State the preparation type.
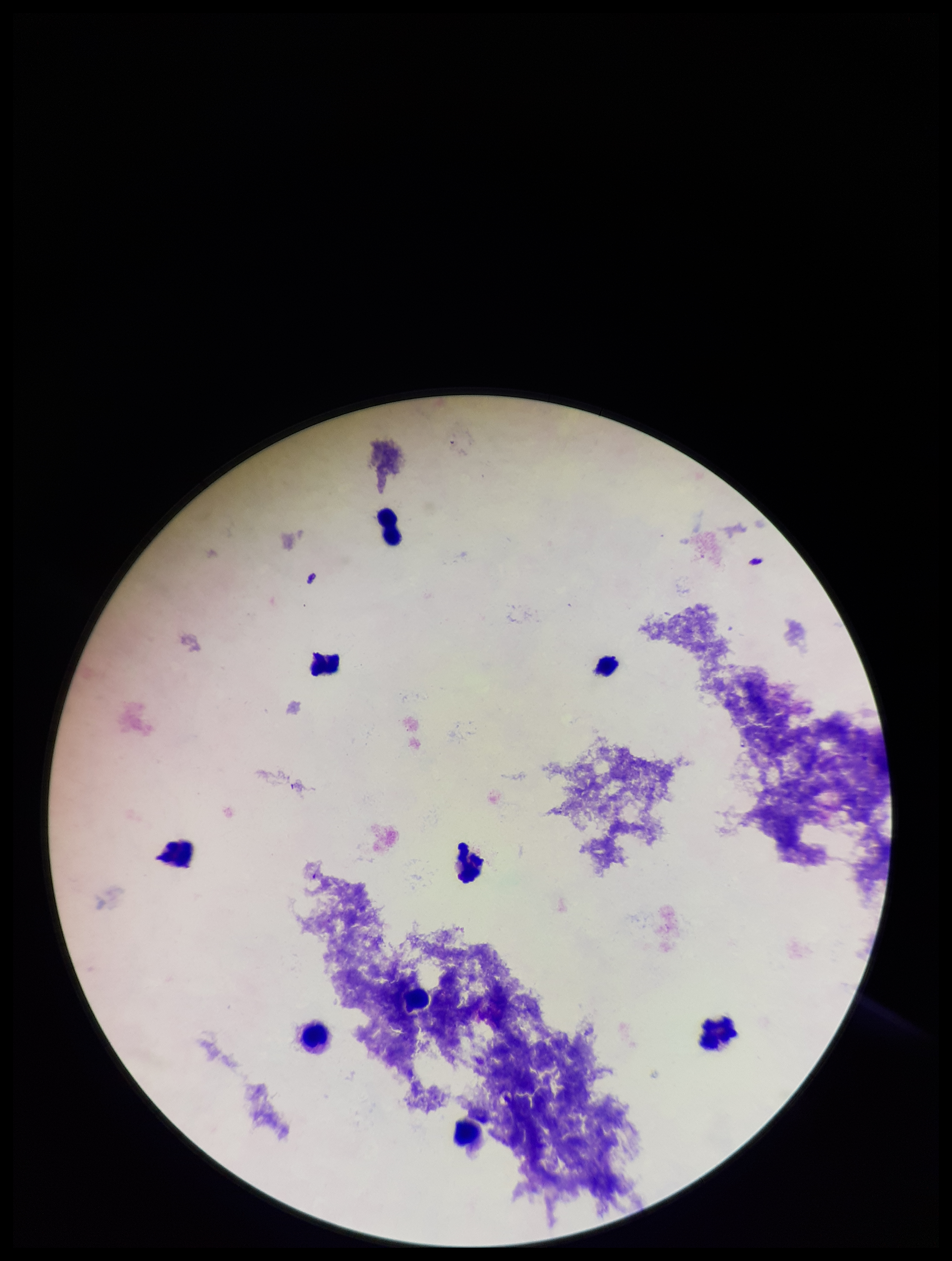
It is a thick blood smear.

Single field of view. Plasmodium parasites: none seen. Patient malaria status: negative. Parasite count: 0. Giemsa stain. Image is 952×1261 pixels. Leukocyte count: 8. Smartphone photograph taken through the eyepiece of a microscope.